Give the position of every leukocyte visible.
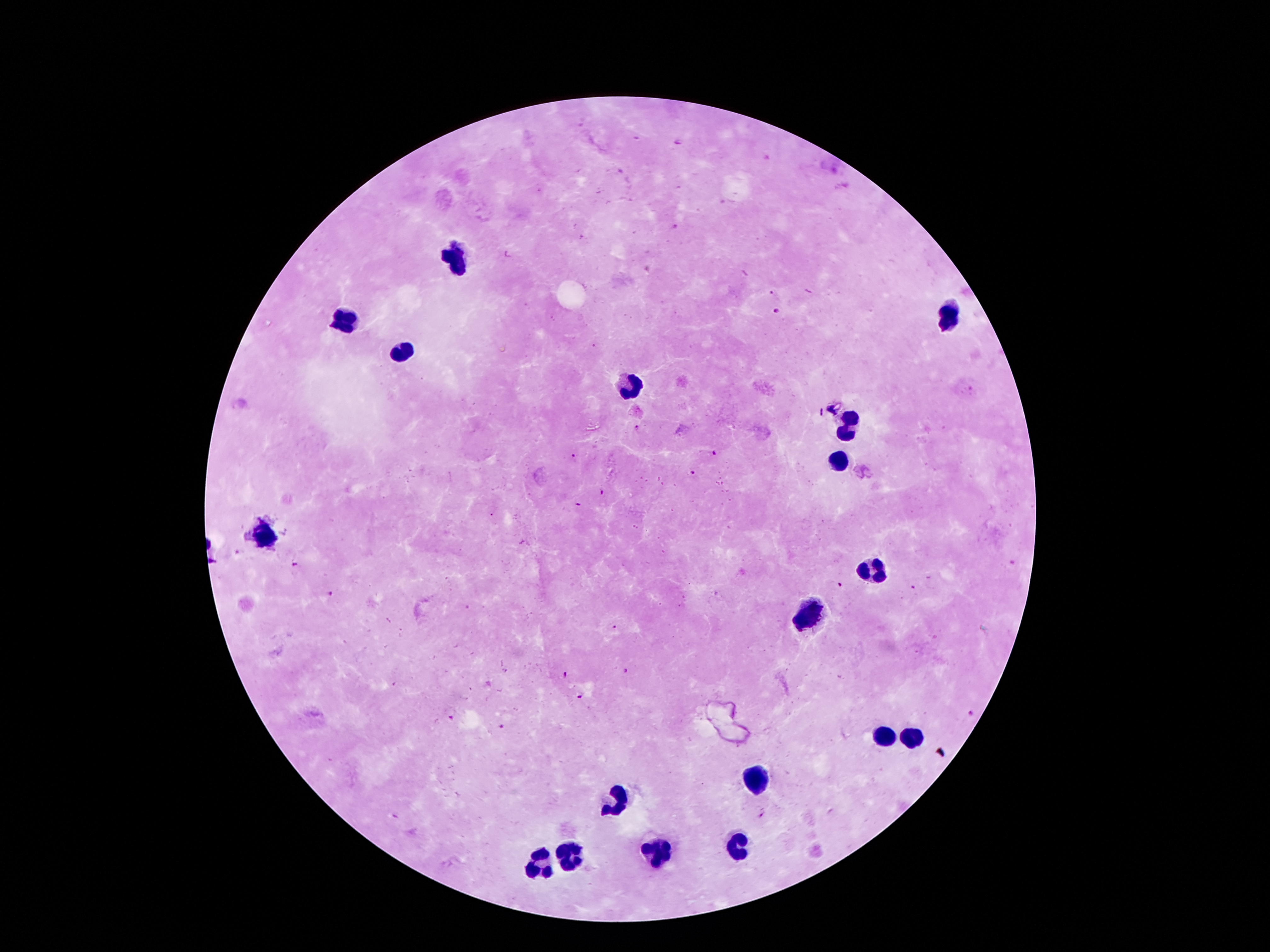

Approximate centers as [x, y] in pixels.
Leukocytes: [455, 258], [946, 316], [342, 321], [402, 350], [627, 385], [848, 426], [837, 462], [262, 535], [875, 571], [808, 614], [886, 735], [912, 737], [757, 781], [615, 802], [736, 850], [660, 852], [571, 855], [542, 861].

Malaria parasite locations: [681, 142], [676, 225], [774, 291], [776, 312], [635, 428], [715, 452], [573, 456], [692, 472], [601, 493], [578, 504], [238, 553], [296, 564], [840, 585], [912, 588], [328, 592], [613, 627], [625, 670], [566, 674], [581, 697], [969, 712], [453, 719], [501, 725], [763, 815]. Thick blood film. Photographed through the microscope eyepiece with a smartphone camera. Image is 1270×952 pixels. One field from this slide. 100x magnification. Giemsa-stained preparation. Patient malaria status: infected with Plasmodium falciparum.